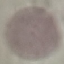
Summary:
  - Result: no malaria parasites detected
  - Stain: Giemsa
  - Capture: smartphone camera at the microscope eyepiece
  - Preparation: thin blood smear
  - Image type: automatically extracted cell patch, resized to 64 × 64 pixels